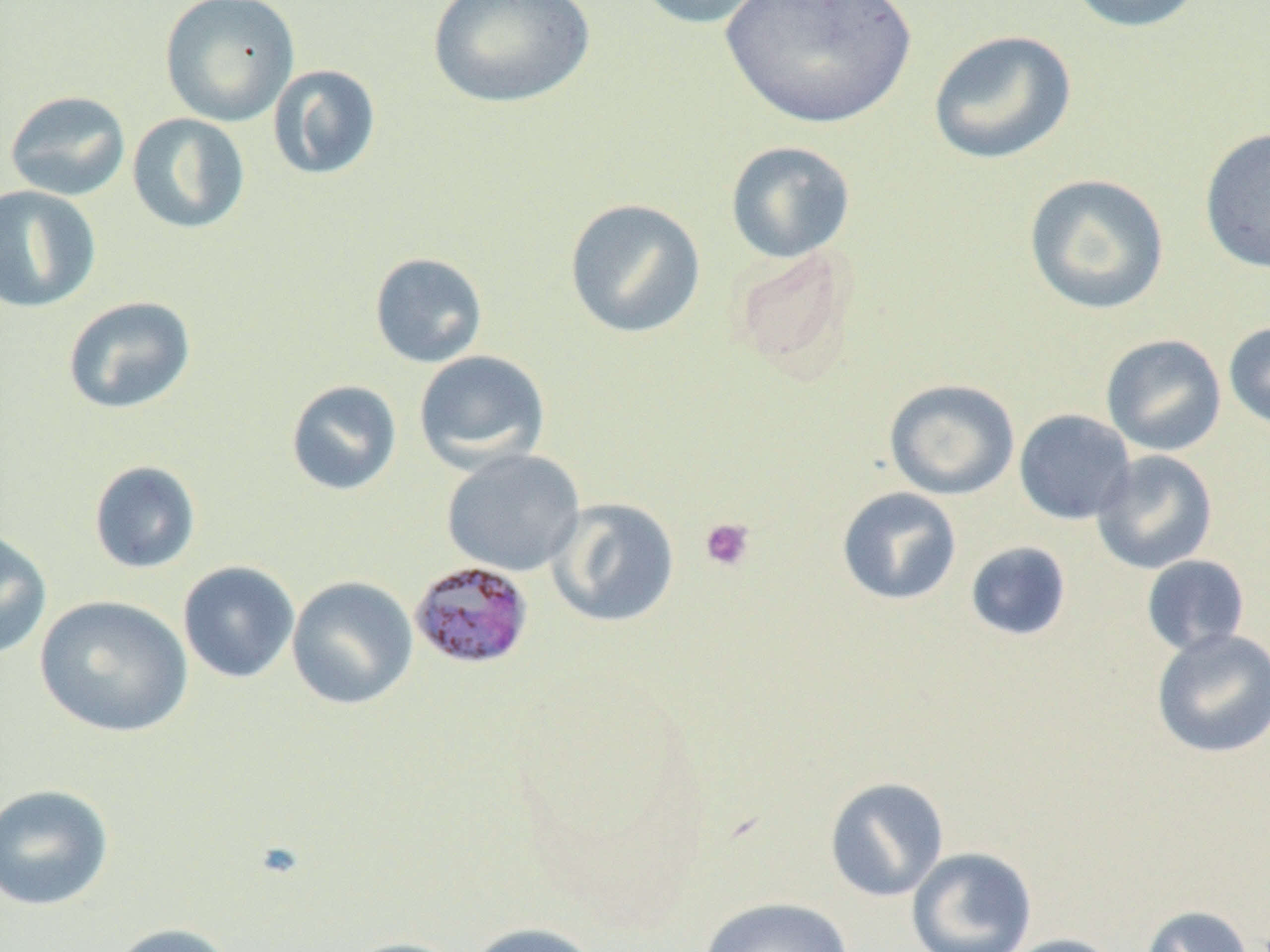

Summary:
  - Coordinate format: approximate bounding boxes as (x1, y1, x2, y2) in pixels
  - Plasmodium malariae-infected red blood cell locations: (408, 559, 535, 671)
  - Uninfected red blood cell locations: (158, 0, 300, 128), (427, 0, 596, 109), (632, 0, 772, 30), (715, 0, 921, 130), (1064, 0, 1210, 34), (927, 29, 1077, 166), (267, 64, 382, 181), (4, 90, 131, 202), (126, 113, 251, 235), (1199, 126, 1270, 275), (725, 140, 856, 264), (1023, 173, 1171, 315), (0, 185, 101, 313), (564, 197, 706, 339), (729, 244, 860, 381), (369, 252, 489, 368), (63, 296, 196, 414), (1223, 320, 1270, 434), (1100, 334, 1226, 456), (413, 350, 550, 473), (883, 378, 1020, 500), (285, 379, 402, 496), (1014, 409, 1136, 525), (441, 448, 585, 577), (1091, 449, 1218, 574), (88, 460, 202, 574), (836, 486, 962, 605), (545, 497, 680, 628), (0, 528, 52, 661), (964, 541, 1072, 642), (1141, 555, 1250, 657), (177, 560, 301, 683), (286, 575, 419, 710), (34, 595, 193, 737), (1151, 628, 1270, 759), (824, 776, 949, 902), (0, 783, 115, 912), (906, 847, 1037, 952), (698, 896, 853, 952), (1140, 905, 1255, 952), (107, 921, 239, 952), (464, 921, 605, 952), (999, 934, 1127, 952), (338, 936, 470, 952)
  - Platelet locations: (699, 518, 756, 572)
  - Slide-level diagnosis: Plasmodium malariae
  - Image size: 1270×952 pixels
  - Modality: optical microscopy
  - Magnification: 1000x
  - Field of view: single
  - Preparation: thin blood film